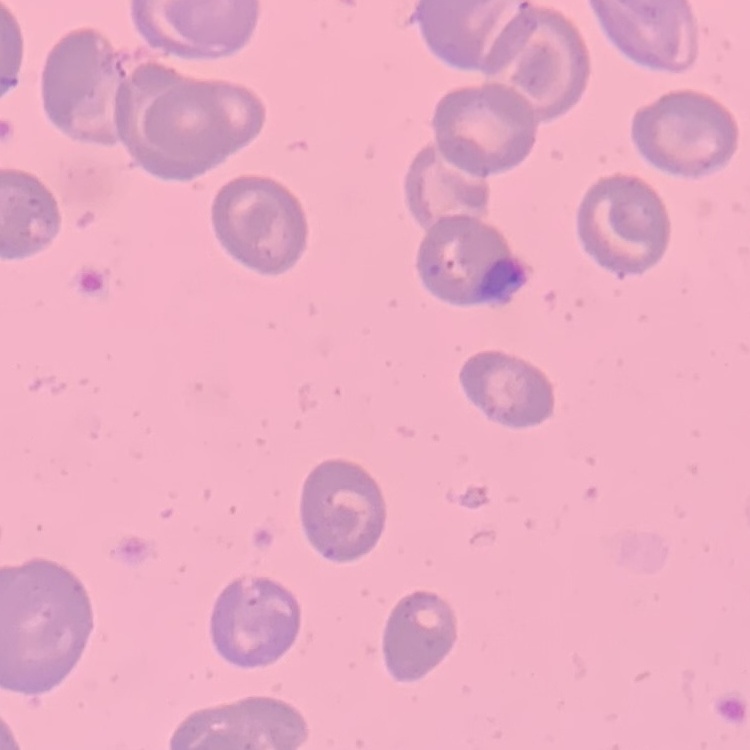 The erythrocytes show no rouleaux formation. Square crop of a larger photomicrograph. Thin blood film. Stained with either Field's or Giemsa.